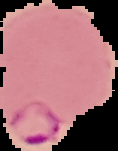
Segmented cell region on a black background. From a thin blood smear. Malaria status: parasitized. Image is 118×151 pixels.